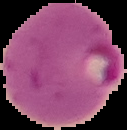
Summary:
  - Malaria status: parasitized
  - Image size: 127×130 pixels
  - Image type: cell region segmented out of the field of view; surrounding area masked to black
  - Preparation: thin blood smear